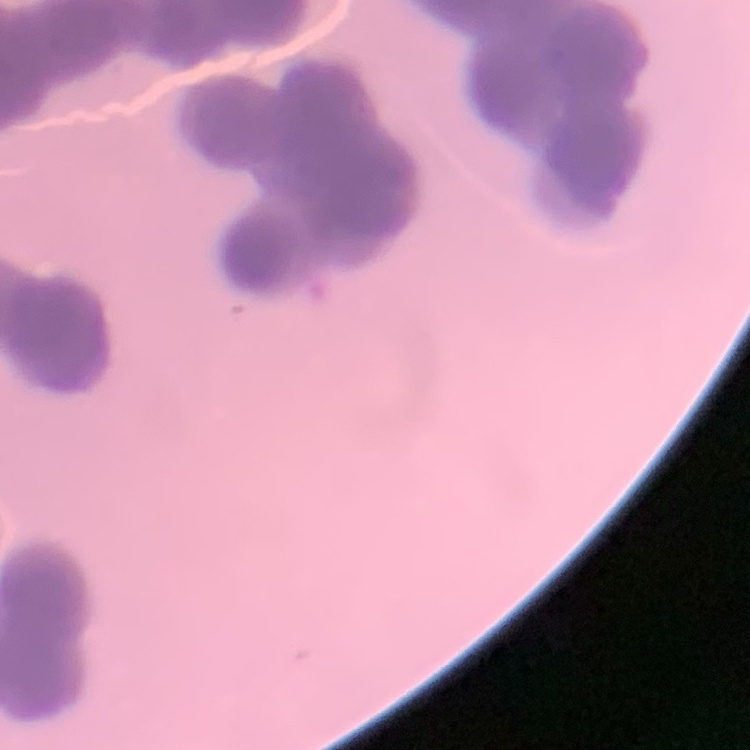

red blood cell morphology = rouleaux formation
image type = one tile cut from a larger photomicrograph
preparation = thin blood smear
stain = Field's or Giemsa